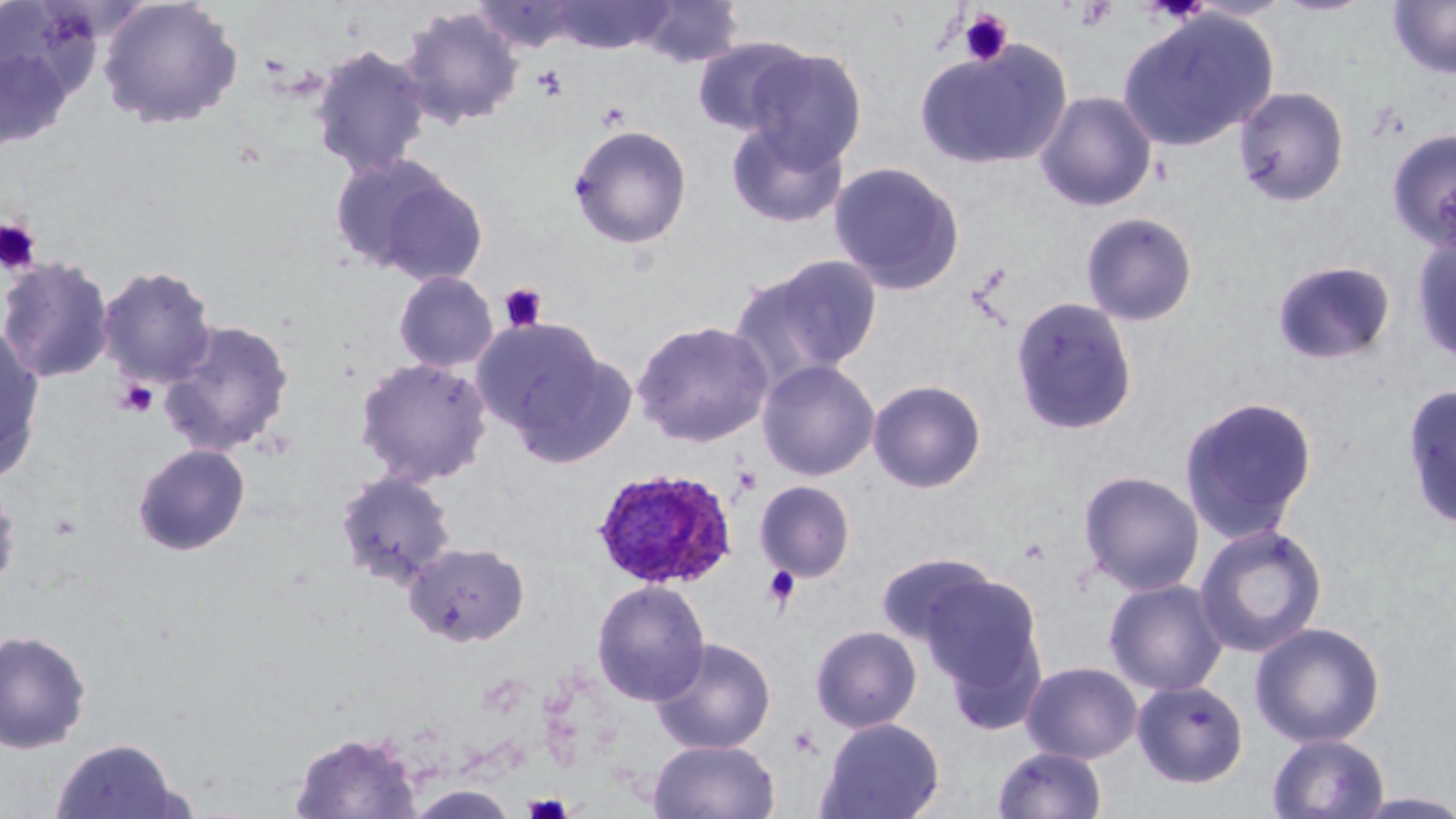
{
  "slide_level_diagnosis": "Plasmodium ovale",
  "stain": "May-Grünwald-Giemsa",
  "modality": "optical microscopy",
  "preparation": "thin blood smear",
  "platelet_locations": "approximate bounding boxes as (x1, y1, x2, y2) in pixels: (1074, 1, 1116, 33), (957, 9, 1014, 66), (532, 64, 568, 100), (0, 218, 41, 274), (498, 281, 548, 333), (113, 378, 159, 419), (732, 465, 763, 496), (762, 566, 800, 611), (787, 726, 823, 760), (522, 793, 576, 818)",
  "plasmodium_ovale_infected_red_blood_cell_locations": "approximate bounding boxes as (x1, y1, x2, y2) in pixels: (591, 467, 738, 590)",
  "magnification": "1000x",
  "field_of_view": "single",
  "uninfected_red_blood_cell_locations": "approximate bounding boxes as (x1, y1, x2, y2) in pixels: (98, 0, 244, 130), (549, 0, 672, 54), (632, 0, 745, 69), (474, 1, 579, 53), (1387, 1, 1456, 80), (398, 6, 524, 129), (1116, 9, 1277, 153), (691, 37, 810, 137), (0, 41, 76, 154), (914, 41, 1072, 171), (310, 45, 431, 179), (744, 48, 868, 168), (1234, 86, 1350, 207), (1034, 90, 1158, 212), (725, 120, 849, 229), (569, 123, 693, 249), (1386, 128, 1456, 250), (329, 152, 465, 277), (829, 160, 966, 296), (1080, 212, 1199, 327), (1411, 231, 1456, 365), (737, 254, 883, 379), (0, 255, 115, 384), (1272, 260, 1396, 366), (98, 265, 218, 388), (393, 270, 499, 373), (1009, 296, 1139, 436), (472, 316, 617, 450), (158, 318, 295, 457), (632, 320, 774, 448), (0, 323, 46, 483), (355, 356, 492, 486), (757, 359, 880, 481), (867, 379, 987, 493), (1401, 384, 1456, 532), (1178, 394, 1318, 543), (132, 443, 251, 557), (334, 470, 458, 589), (1078, 470, 1205, 595), (754, 480, 856, 582), (0, 482, 22, 594), (1193, 523, 1328, 657), (404, 541, 530, 648), (875, 552, 1000, 650), (917, 572, 1048, 711), (1104, 578, 1229, 696), (591, 579, 710, 706), (1249, 621, 1386, 747), (810, 625, 922, 732), (0, 628, 92, 754), (650, 637, 776, 755), (1020, 661, 1142, 763), (1132, 679, 1248, 788), (817, 717, 945, 819), (289, 729, 423, 818), (1266, 732, 1390, 819), (49, 737, 191, 819), (648, 739, 780, 819), (992, 745, 1108, 819), (404, 784, 522, 818), (1348, 791, 1456, 818)",
  "image_size": "1456×819 pixels"
}